Classify this cell by malaria status.
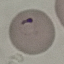
It is parasitized.

Summary:
  - Preparation: thin blood film
  - Capture: smartphone through the microscope eyepiece
  - Image type: cell patch, automatically extracted from a larger field of view and resized to 64 × 64 pixels
  - Stain: Giemsa